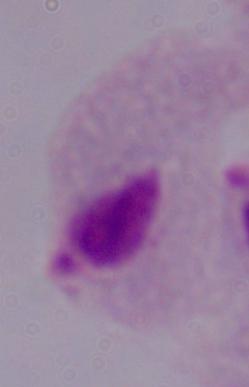
A trichomonad is seen. Photomicrograph. 1000x magnification.